State the blood parasite species.
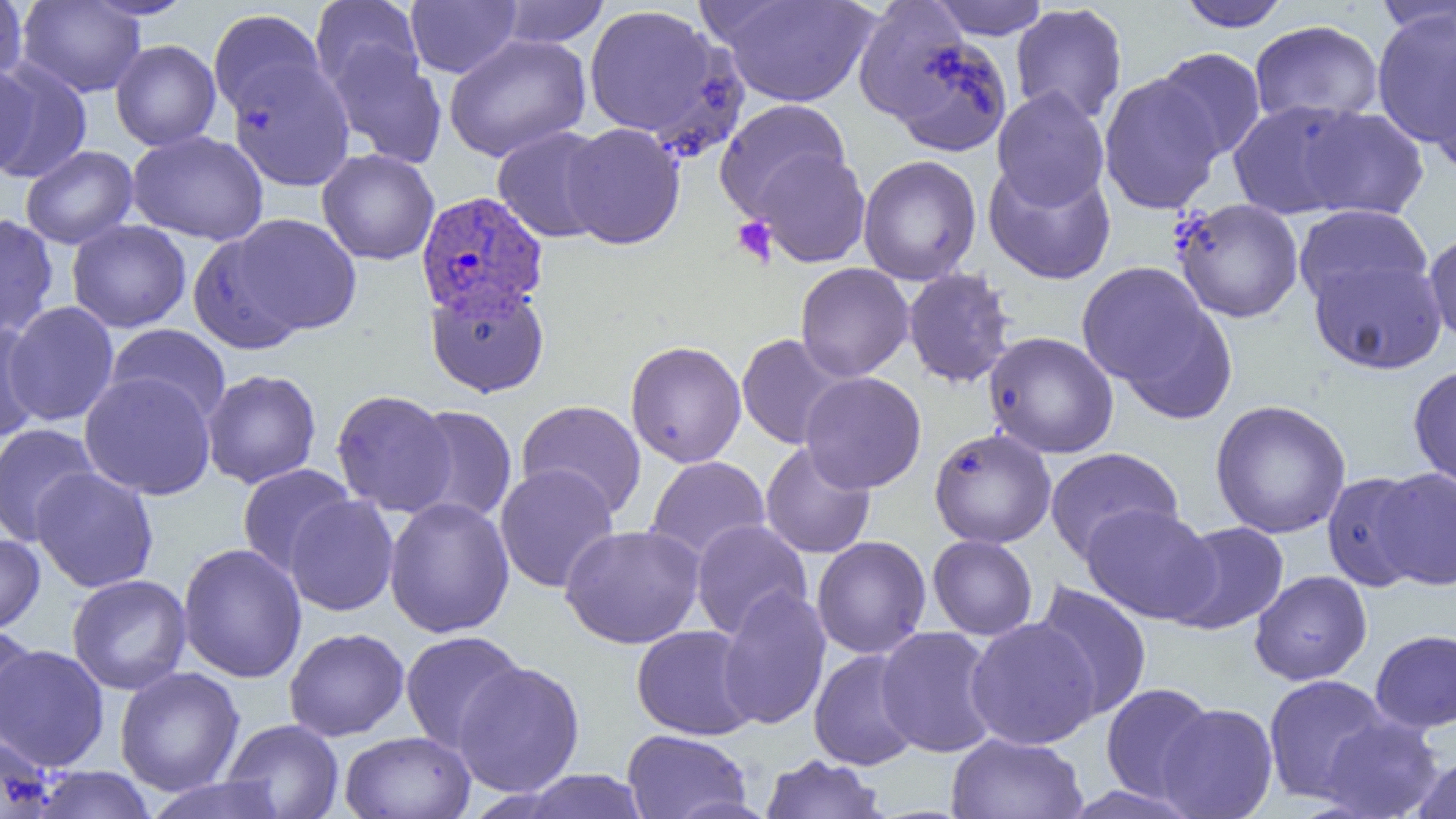
Plasmodium vivax.

Approximate bounding boxes as (x1, y1, x2, y2) in pixels. Platelet locations: (731, 216, 778, 267). Plasmodium vivax-infected red blood cell locations: (419, 189, 552, 318). Uninfected red blood cell locations: (0, 0, 27, 84), (81, 0, 197, 20), (310, 0, 424, 95), (405, 0, 521, 78), (711, 0, 880, 108), (853, 0, 981, 132), (927, 0, 1052, 40), (1176, 0, 1294, 32), (16, 1, 147, 97), (495, 1, 611, 48), (1374, 1, 1455, 39), (1010, 3, 1128, 124), (584, 4, 722, 140), (1371, 7, 1456, 151), (208, 9, 325, 119), (1250, 19, 1384, 126), (879, 28, 1013, 157), (443, 34, 592, 162), (110, 39, 221, 151), (328, 45, 447, 168), (1153, 47, 1267, 162), (1429, 49, 1456, 179), (0, 61, 93, 182), (228, 61, 355, 190), (0, 62, 42, 178), (1099, 74, 1224, 215), (992, 88, 1110, 210), (714, 98, 851, 221), (1228, 99, 1366, 219), (1296, 106, 1429, 221), (561, 123, 685, 250), (492, 125, 613, 243), (127, 130, 268, 245), (20, 145, 138, 249), (751, 148, 871, 268), (317, 149, 440, 265), (858, 154, 982, 285), (983, 160, 1117, 285), (1170, 198, 1305, 324), (1293, 204, 1432, 310), (0, 213, 59, 338), (230, 213, 362, 336), (66, 219, 191, 333), (1423, 229, 1456, 349), (188, 232, 305, 355), (1308, 255, 1448, 374), (1076, 261, 1222, 400), (795, 262, 914, 382), (902, 267, 1016, 388), (425, 281, 550, 397), (4, 301, 120, 428), (0, 318, 45, 441), (106, 323, 231, 426), (983, 331, 1120, 459), (736, 334, 851, 450), (625, 340, 747, 468), (1408, 364, 1456, 489), (200, 369, 322, 489), (800, 371, 927, 493), (79, 372, 217, 499), (331, 389, 457, 517), (1209, 398, 1352, 539), (516, 400, 647, 519), (404, 405, 518, 526), (0, 423, 101, 545), (929, 428, 1057, 548), (760, 442, 876, 559), (1044, 447, 1183, 563), (645, 456, 770, 565), (237, 464, 356, 577), (494, 464, 619, 593), (31, 467, 159, 593), (1372, 467, 1456, 591), (1322, 471, 1427, 593), (284, 495, 399, 616), (384, 497, 515, 638), (1081, 504, 1219, 624), (690, 519, 812, 640), (1165, 520, 1290, 635), (559, 524, 706, 649), (0, 533, 46, 636), (928, 534, 1038, 640), (812, 536, 931, 659), (177, 542, 307, 683), (1249, 570, 1373, 685), (67, 574, 192, 696), (1031, 581, 1152, 720), (716, 586, 831, 730), (965, 617, 1102, 750), (631, 624, 758, 740), (0, 625, 40, 746), (876, 626, 1000, 757), (284, 627, 409, 741), (1370, 629, 1456, 733), (400, 631, 526, 753), (0, 644, 110, 771), (809, 649, 922, 771), (453, 661, 585, 797), (114, 667, 245, 796), (1263, 674, 1392, 804), (1100, 683, 1217, 803), (1156, 703, 1278, 819), (1317, 714, 1444, 819), (221, 718, 345, 818), (622, 729, 752, 819), (340, 730, 476, 819), (0, 732, 59, 819), (946, 732, 1088, 818), (1412, 752, 1456, 819), (760, 754, 887, 818), (27, 766, 158, 819), (516, 769, 651, 819), (142, 775, 289, 819), (1057, 784, 1205, 819). Thin blood film. One field of a larger specimen. 1000x magnification. Image is 1456×819 pixels. Light microscopy.